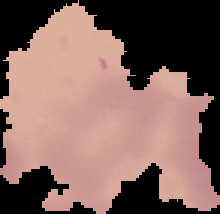

Image is 220×214 pixels. Segmented cell region on a black background. From a thin blood smear. Malaria status: uninfected.